Assess the background quality.
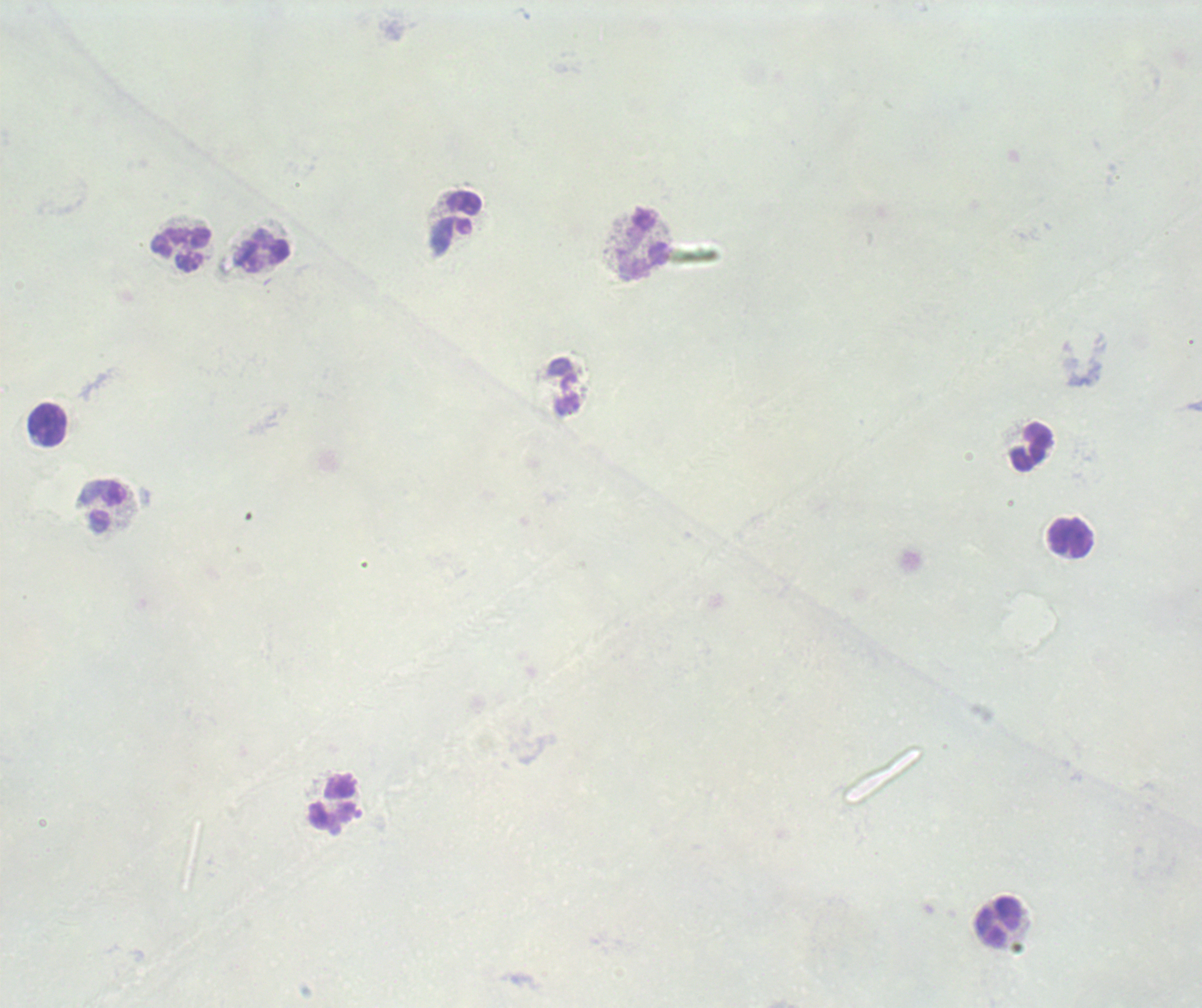
It is poor.

Approximate object centers, in pixels from the top-left corner. Leukocyte locations: (x=462, y=214), (x=644, y=244), (x=181, y=249), (x=263, y=251), (x=563, y=388), (x=47, y=425), (x=1032, y=447), (x=103, y=507), (x=1071, y=538), (x=335, y=803), (x=999, y=922). Image is 1202×1008 pixels. 100x magnification. Result: no Plasmodium parasites detected. Previously used in an actual diagnosis. Romanowsky-stained preparation. Thick blood smear. One field from this slide.